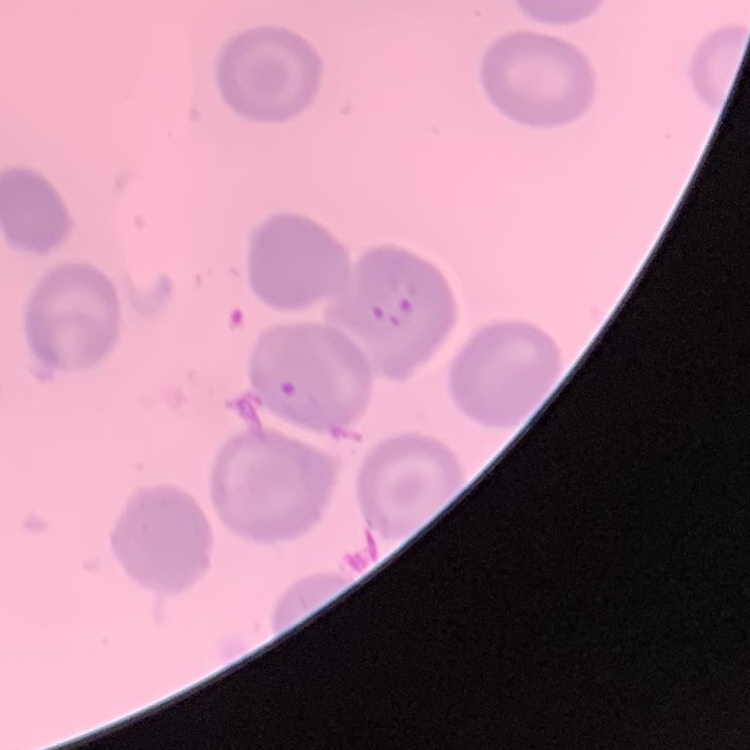 The red blood cells exhibit no rouleaux formation. Thin blood film. Field's or Giemsa stain. Square crop of a larger photomicrograph.